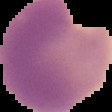
From a thin blood smear. Malaria status: parasitized. Image is 112×112 pixels. The area outside the segmented cell region is set to black.